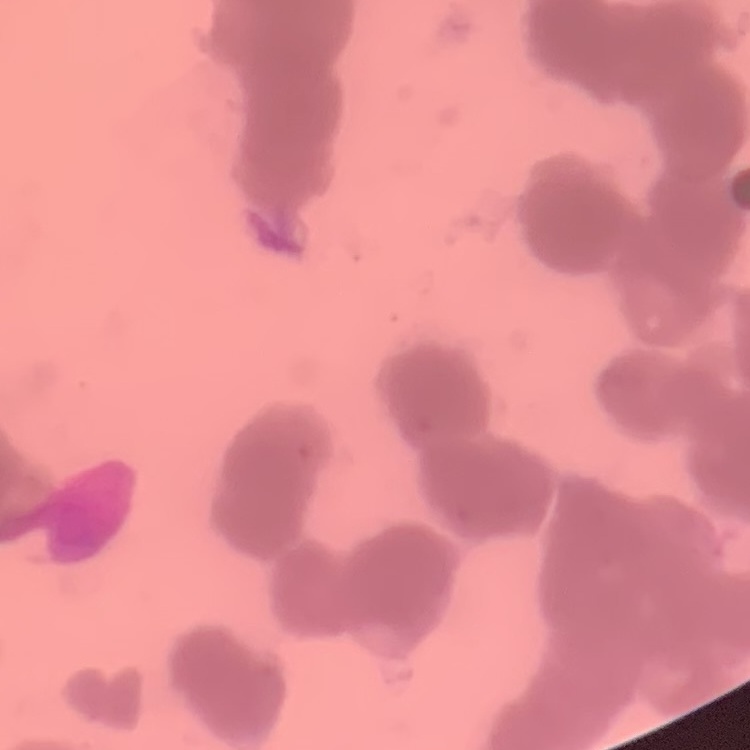
Summary:
  - Red blood cell morphology: rouleaux formation
  - Preparation: thin blood film
  - Image type: one tile cut from a larger photomicrograph
  - Stain: Field's or Giemsa